Describe the morphology of the erythrocytes.
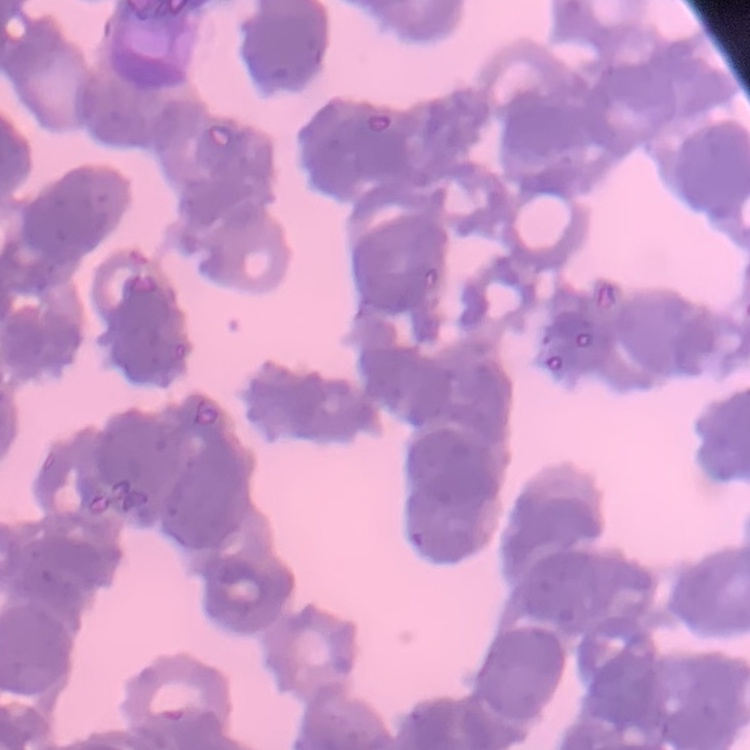

Rouleaux formation.

Summary:
  - Preparation: thin blood smear
  - Image type: square crop of a larger photomicrograph
  - Stain: Field's or Giemsa